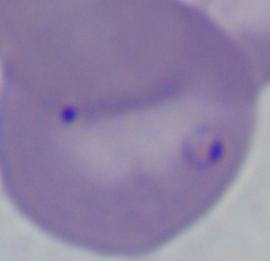
Micrograph. A Babesia parasite is shown. Captured at 1000x magnification.